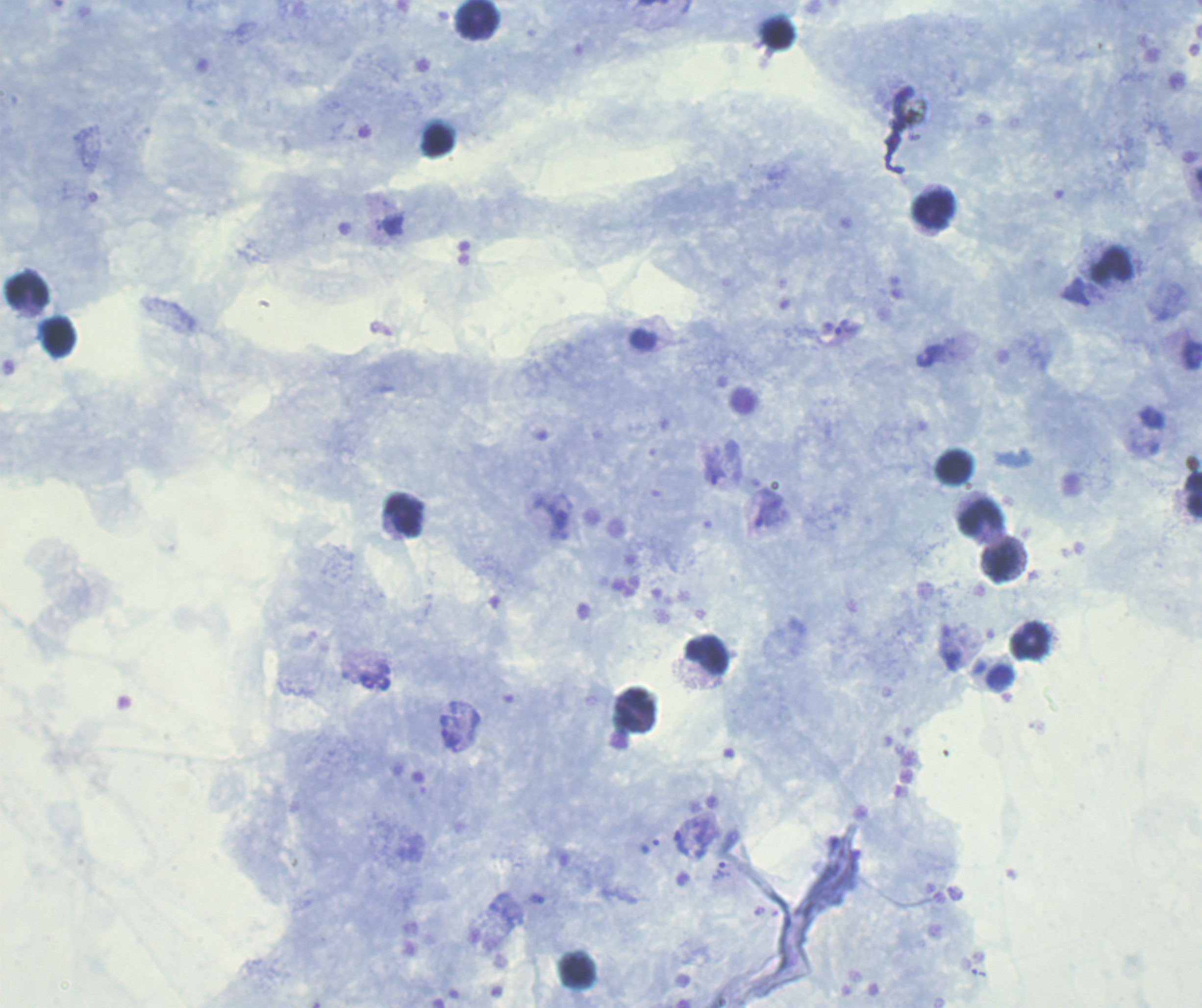

{
  "field_of_view": "one from this slide",
  "preparation": "thick smear of blood",
  "image_size": "1202×1008 pixels",
  "stain": "Romanowsky",
  "result": "positive for malaria parasites",
  "trophozoite_locations": "approximate centers as {x, y} in pixels: {847, 327}, {714, 470}, {769, 512}, {451, 737}, {683, 843}, {721, 870}",
  "background_quality": "good",
  "magnification": "100x",
  "leukocyte_locations": "approximate centers as {x, y} in pixels: {478, 19}, {934, 210}, {1113, 264}, {27, 291}, {59, 337}, {955, 467}, {1194, 495}, {980, 518}, {1001, 563}, {1031, 641}, {707, 654}",
  "coloration_quality": "good",
  "context": "previously used in a real diagnosis"
}